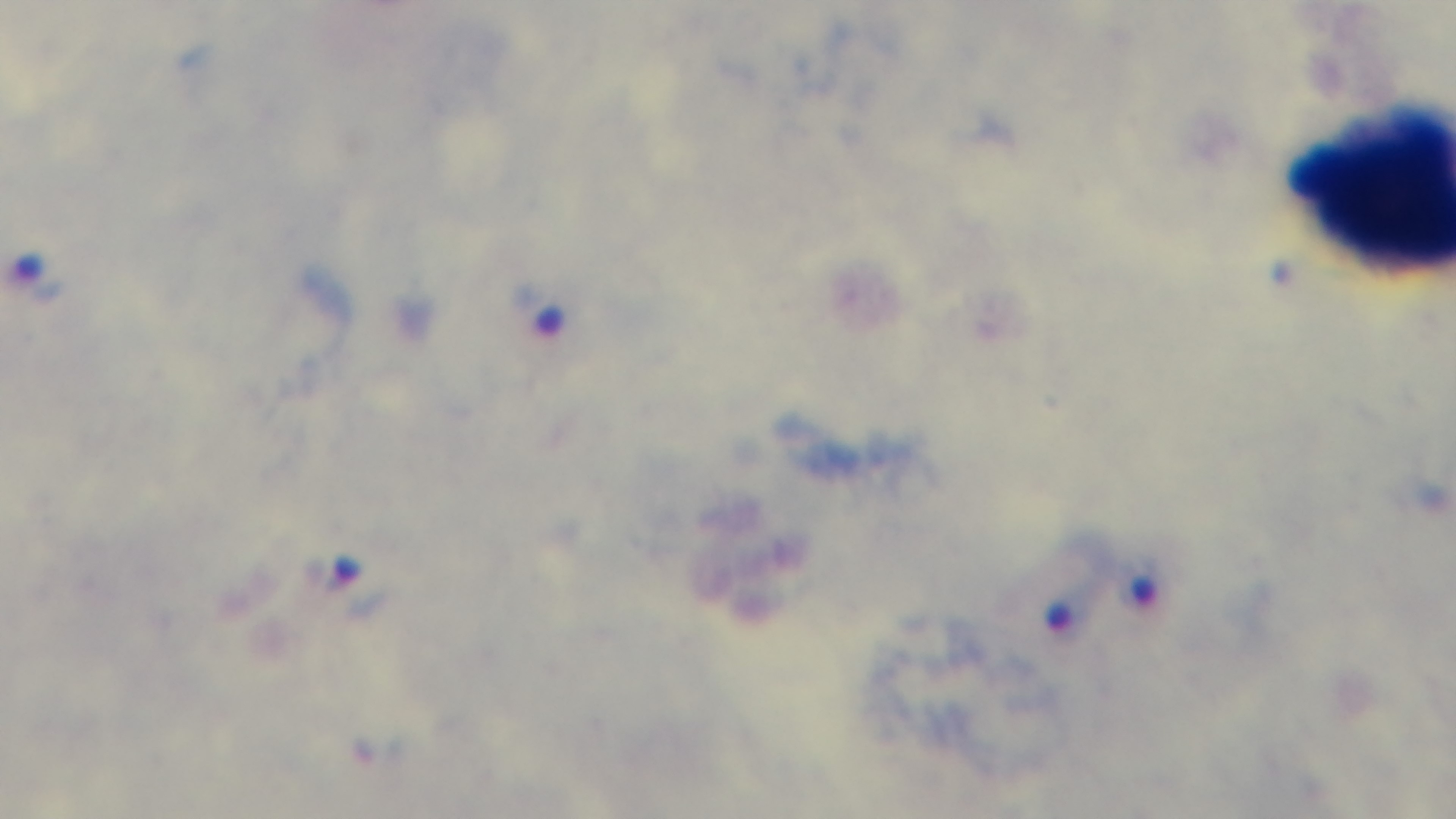

objective = 100x oil immersion
field of view = one from the slide
stain = Giemsa
modality = light microscopy
malaria status = infected
capture = mounted 4K digital camera
preparation = thick smear